Identify the parasite.
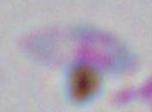
Toxoplasma gondii.

Micrograph. Captured at 1000x magnification.